Classify the preparation.
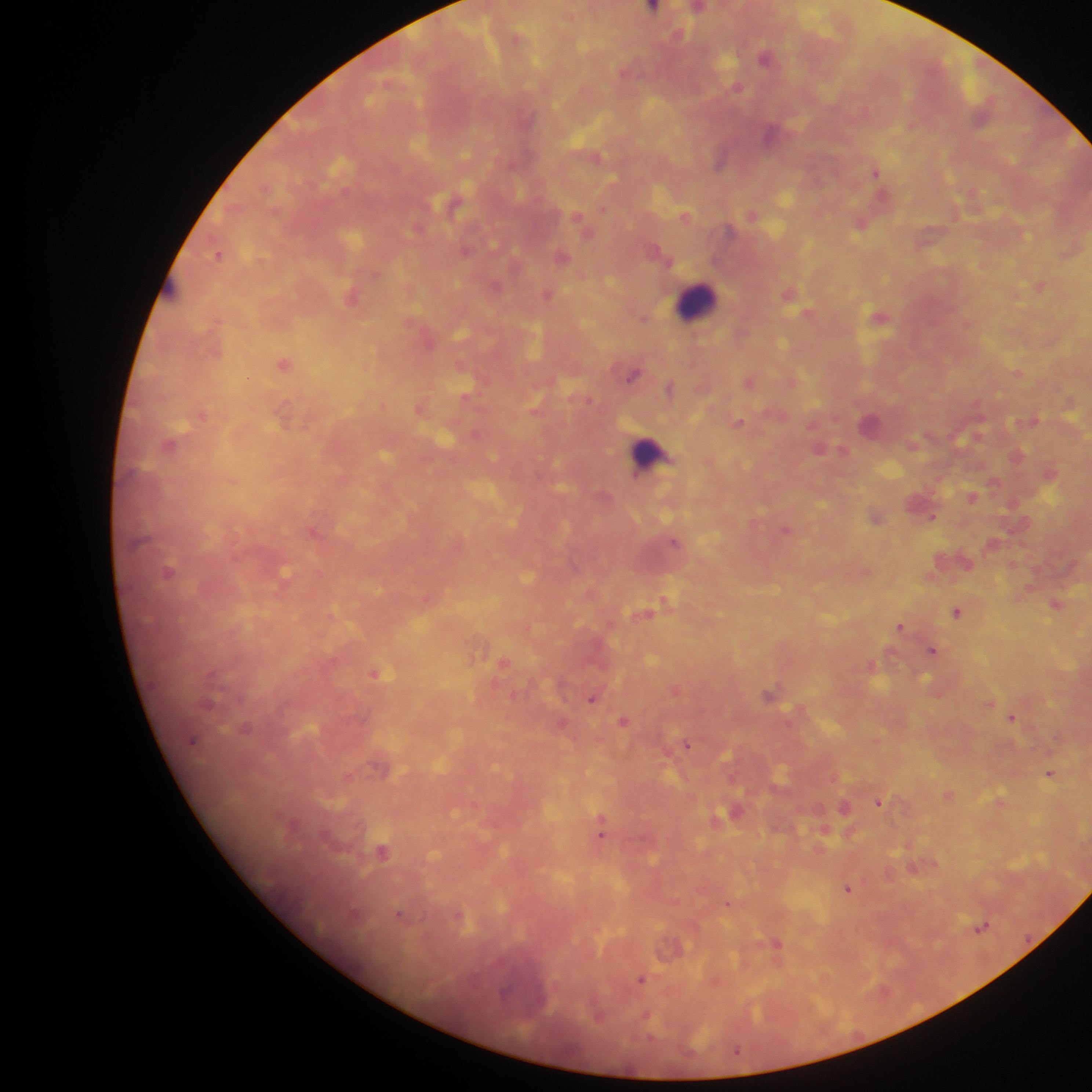

Thick blood smear.

Approximate centers as {x, y} in pixels.
Summary:
  - Malaria parasite locations: {653, 7}, {698, 7}, {678, 34}, {517, 38}, {766, 56}, {737, 87}, {721, 160}, {876, 171}, {453, 203}, {603, 208}, {753, 213}, {686, 216}, {578, 218}, {862, 222}, {466, 250}, {220, 254}, {563, 255}, {664, 256}, {1040, 285}, {496, 286}, {548, 293}, {789, 293}, {352, 296}, {808, 312}, {645, 317}, {880, 317}, {284, 363}, {1017, 372}, {633, 374}, {749, 381}, {670, 388}, {468, 396}, {1071, 401}, {421, 408}, {284, 414}, {203, 415}, {738, 422}, {870, 423}, {170, 445}, {842, 450}, {1018, 456}, {994, 480}, {973, 496}, {877, 516}, {933, 516}, {786, 529}, {314, 531}, {675, 542}, {964, 560}, {168, 573}, {284, 576}, {429, 598}, {665, 601}, {1056, 604}, {651, 610}, {958, 611}, {901, 627}, {934, 651}, {504, 662}, {872, 664}, {375, 674}, {676, 689}, {770, 694}, {593, 698}, {1012, 716}, {624, 721}, {687, 745}, {1049, 773}, {949, 794}, {880, 801}, {1001, 802}, {845, 806}, {734, 812}, {719, 819}, {602, 827}, {825, 830}, {382, 852}, {914, 868}, {848, 888}, {728, 904}, {401, 916}, {459, 916}, {981, 926}, {777, 944}, {641, 980}, {648, 1016}, {737, 1050}
  - Leukocyte locations: {170, 289}, {695, 301}, {649, 453}
  - Field of view: single
  - Image size: 1092×1092 pixels
  - Capture: mobile-phone photograph through a microscope
  - Country: Ghana